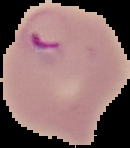

Summary:
  - Image type: segmented cell region on a black background
  - Preparation: thin blood smear
  - Image size: 130×148 pixels
  - Result: malaria parasites detected